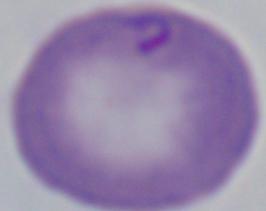
identification: Babesia
magnification: 1000x
modality: photomicrograph